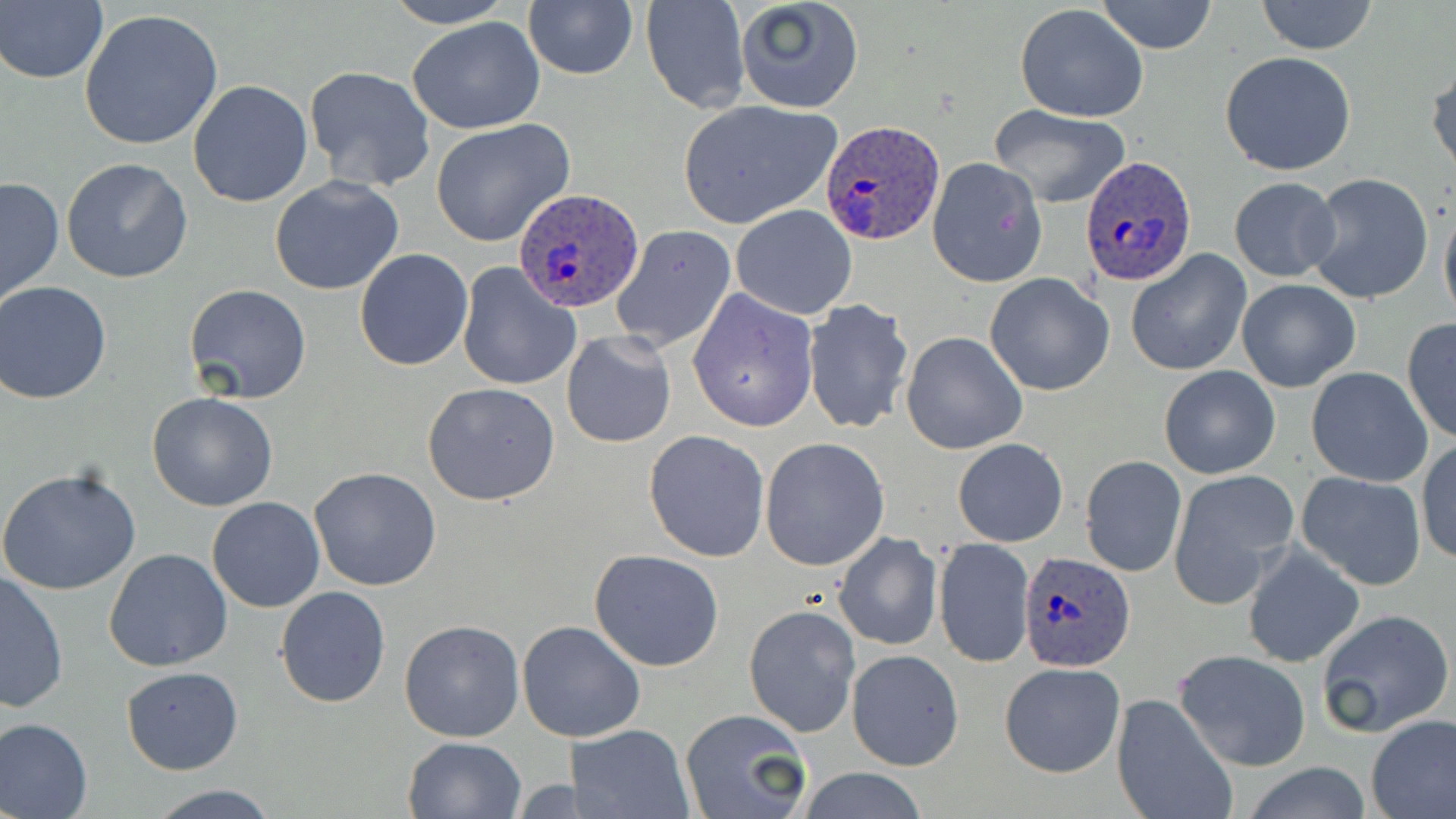
slide-level diagnosis = Plasmodium ovale
field of view = single
magnification = 1000x
preparation = thin blood smear
image size = 1456×819 pixels
Plasmodium ovale-infected red blood cell locations = approximate bounding boxes as (x1,y1)-(x2,y2) corner pairs in pixels: (819,119)-(946,245), (1080,155)-(1198,288), (511,188)-(643,312), (1020,551)-(1139,672)
modality = optical microscopy
uninfected red blood cell locations = approximate bounding boxes as (x1,y1)-(x2,y2) corner pairs in pixels: (380,0)-(517,29), (734,0)-(864,114), (1097,0)-(1218,54), (1256,0)-(1379,55), (523,1)-(638,81), (641,1)-(750,113), (1,2)-(109,85), (1015,5)-(1148,124), (79,8)-(226,151), (406,17)-(547,134), (1219,51)-(1357,175), (1428,59)-(1456,181), (304,65)-(436,193), (187,80)-(313,208), (678,101)-(840,229), (988,105)-(1132,209), (430,119)-(576,249), (62,157)-(194,284), (927,157)-(1046,287), (1306,173)-(1434,304), (0,175)-(64,310), (269,175)-(404,296), (1229,176)-(1340,282), (1439,198)-(1456,329), (730,204)-(858,319), (610,224)-(736,354), (354,248)-(473,370), (1126,251)-(1252,376), (455,261)-(582,392), (985,273)-(1114,395), (1236,279)-(1361,392), (0,281)-(116,404), (184,284)-(312,404), (687,289)-(818,433), (802,299)-(915,434), (801,314)-(1026,442), (1401,319)-(1456,443), (561,331)-(677,449), (902,332)-(1028,455), (1159,365)-(1280,479), (1305,366)-(1434,488), (422,382)-(561,505), (147,391)-(279,512), (643,429)-(770,561), (760,438)-(890,571), (952,438)-(1068,547), (1416,438)-(1455,566), (1080,455)-(1186,577), (309,467)-(442,592), (0,468)-(142,597), (1169,470)-(1297,606), (1295,471)-(1427,591), (207,496)-(326,612), (833,532)-(942,650), (934,537)-(1034,669), (1241,544)-(1364,669), (103,548)-(233,672), (589,549)-(725,671), (1,571)-(69,713), (275,586)-(391,708), (744,604)-(861,738), (1315,608)-(1455,738), (398,618)-(524,743), (519,621)-(645,742), (846,649)-(964,771), (1174,649)-(1312,771), (1000,662)-(1125,778), (121,666)-(242,775), (1113,691)-(1236,819), (681,709)-(811,819), (1365,715)-(1456,819), (0,717)-(94,818), (571,724)-(693,819), (402,737)-(527,819), (1241,763)-(1374,818), (789,768)-(934,819), (507,777)-(585,815), (145,784)-(279,818)
stain = May-Grünwald-Giemsa